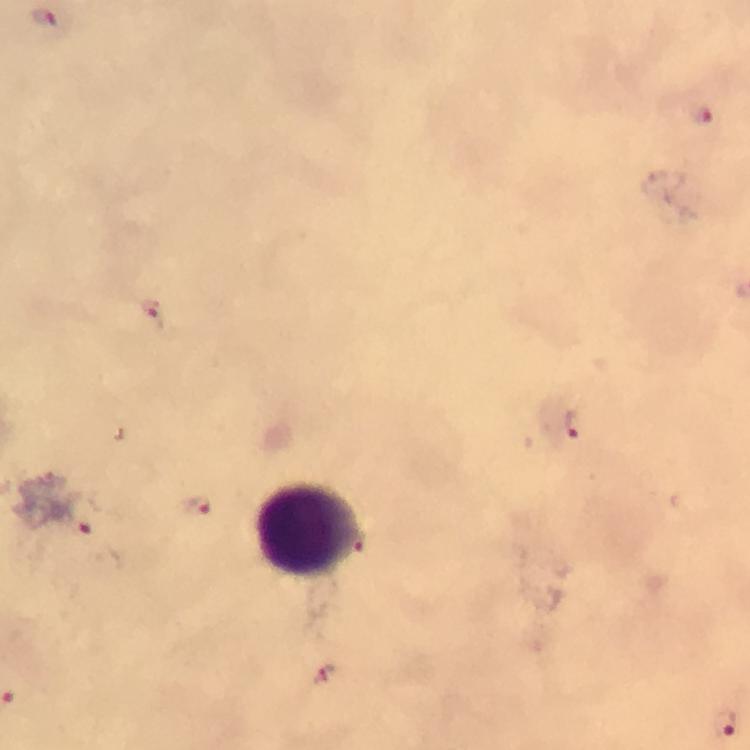

immersion oil = applied
cropped from = a single field of view
stain = Giemsa
preparation = thick blood film
context = from a malaria diagnostic workup
image size = 750×750 pixels
leukocyte locations = approximate centers as (x, y) in pixels: (307, 529)
Plasmodium parasite locations = approximate centers as (x, y) in pixels: (47, 18), (702, 116), (153, 311), (573, 424), (196, 506), (81, 515), (326, 675), (725, 724)
magnification = 100x
capture = smartphone mounted on the microscope